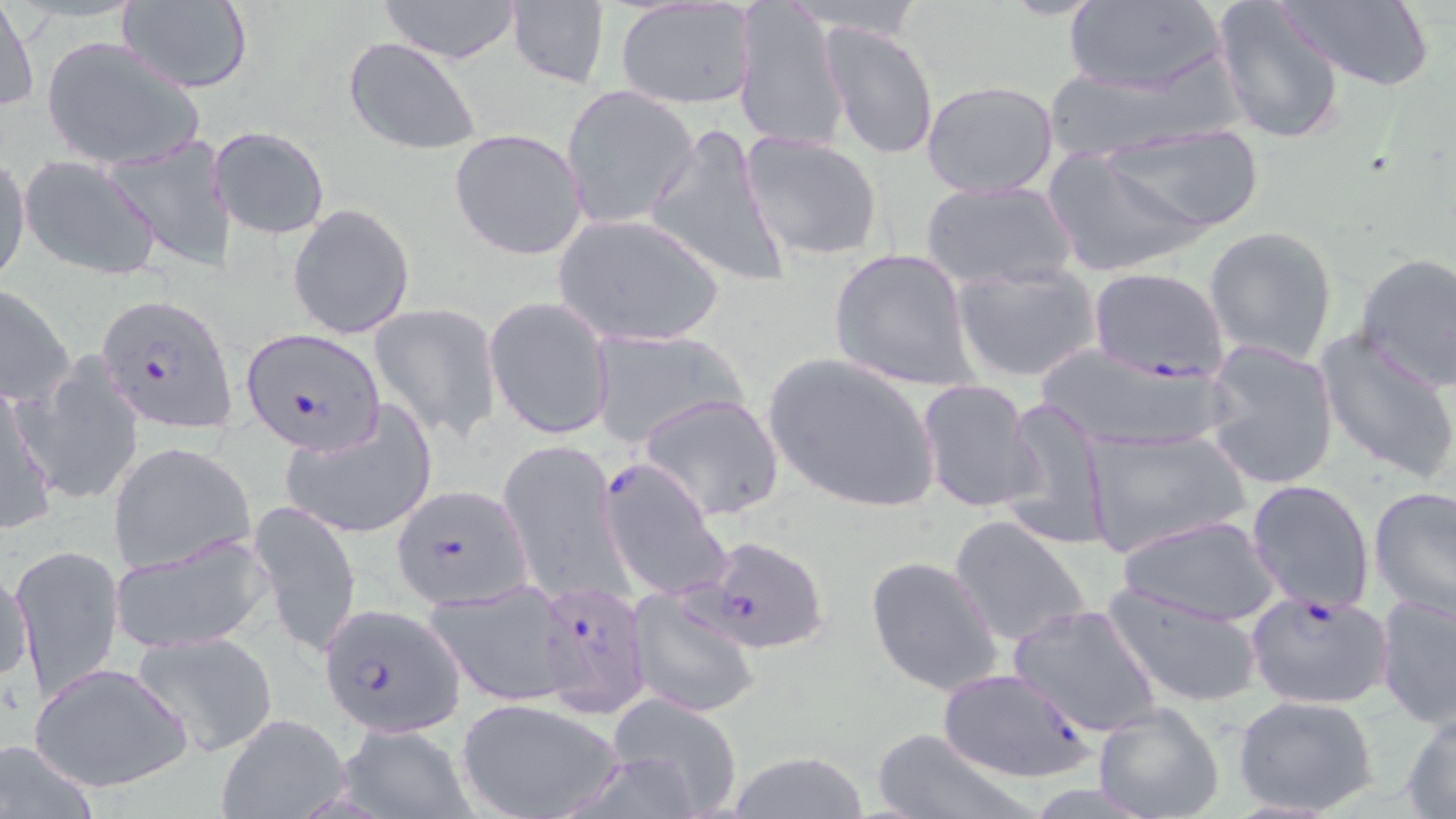

Summary:
  - Coordinate format: approximate bounding boxes as (x1,y1)-(x2,y2) corner pairs in pixels
  - Uninfected red blood cell locations: (1,0)-(38,116), (114,0)-(254,93), (1063,0)-(1227,98), (1212,0)-(1348,144), (378,1)-(523,63), (504,1)-(611,88), (733,1)-(852,155), (1275,1)-(1434,90), (615,2)-(758,110), (823,24)-(939,161), (42,36)-(205,172), (342,37)-(483,158), (1041,67)-(1206,161), (920,80)-(1061,200), (559,84)-(699,231), (1106,121)-(1264,235), (644,122)-(793,287), (208,126)-(329,240), (448,128)-(590,262), (739,131)-(885,263), (105,139)-(234,273), (1044,148)-(1209,278), (0,155)-(33,288), (21,156)-(162,281), (921,179)-(1076,291), (287,204)-(417,341), (553,213)-(726,348), (1203,226)-(1338,364), (830,248)-(975,391), (1354,251)-(1456,391), (951,261)-(1101,383), (0,285)-(76,408), (483,295)-(616,441), (369,302)-(503,443), (588,329)-(745,449), (1315,329)-(1456,483), (1201,342)-(1340,491), (1031,345)-(1230,453), (762,353)-(943,515), (22,356)-(145,507), (0,379)-(59,536), (916,379)-(1042,516), (637,392)-(786,522), (1002,396)-(1113,552), (279,405)-(436,540), (1082,428)-(1249,557), (500,438)-(625,600), (108,440)-(258,575), (1246,479)-(1376,614), (1368,485)-(1455,622), (249,498)-(363,658), (949,514)-(1093,649), (1117,514)-(1283,627), (110,531)-(271,653), (10,542)-(124,700), (865,555)-(1006,697), (3,559)-(36,688), (424,580)-(574,704), (1104,580)-(1266,709), (626,592)-(760,718), (1376,593)-(1456,727), (1007,603)-(1163,737), (131,632)-(277,758), (27,660)-(193,794), (1232,693)-(1380,819), (607,694)-(745,817), (456,697)-(625,819), (1092,702)-(1224,819), (1401,707)-(1456,817), (216,713)-(350,819), (337,724)-(476,817), (870,726)-(1034,819), (1,738)-(101,819), (723,750)-(870,819)
  - Plasmodium falciparum-infected red blood cell locations: (1088,267)-(1230,380), (95,294)-(235,432), (240,329)-(382,455), (597,456)-(731,602), (390,484)-(533,609), (696,538)-(827,655), (532,579)-(650,718), (1245,588)-(1394,711), (317,605)-(465,737), (936,667)-(1095,783)
  - Slide-level diagnosis: Plasmodium falciparum
  - Field of view: single
  - Stain: May-Grünwald-Giemsa
  - Modality: light microscopy
  - Image size: 1456×819 pixels
  - Magnification: 1000x
  - Preparation: thin blood smear